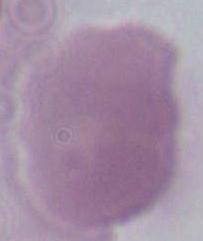 Micrograph. 1000x magnification. A red blood cell is shown.